Report the malaria status of this cell.
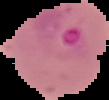
Parasitized.

From a thin blood film. Cell region segmented out of the field of view; the surrounding area is masked to black. Image is 109×100 pixels.